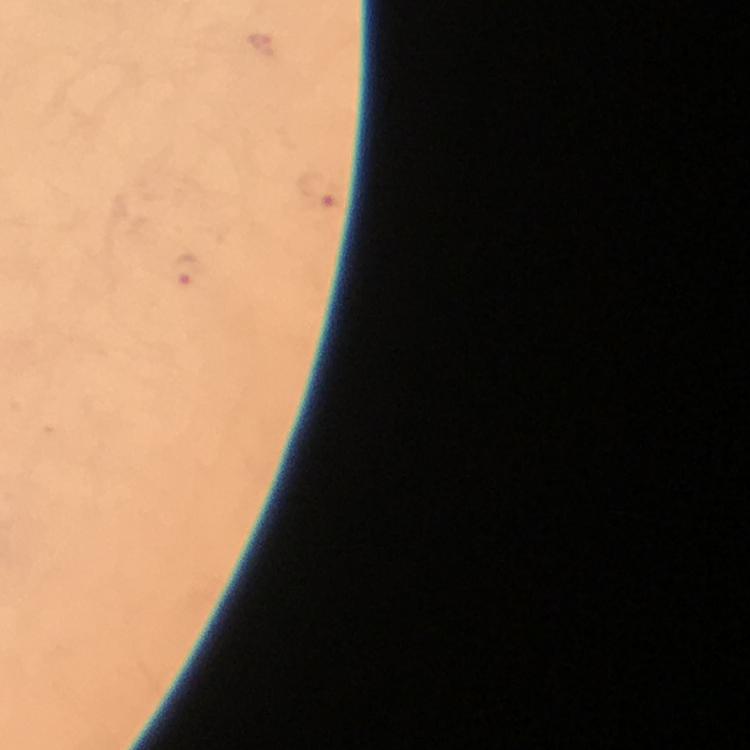
Approximate object centers, in pixels from the top-left corner.
Summary:
  - Plasmodium parasite locations: (x=318, y=191), (x=187, y=272)
  - Image size: 750×750 pixels
  - Context: from a diagnostic examination for malaria
  - Preparation: thick blood smear
  - Magnification: 100x
  - Stain: Giemsa
  - Immersion oil: used
  - Cropped from: one field of view
  - Capture: smartphone mounted on the microscope